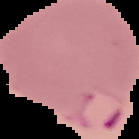
Summary:
  - Preparation: thin blood smear
  - Image size: 139×139 pixels
  - Image type: cell region segmented out of the field of view; surrounding area masked to black
  - Result: Plasmodium parasites identified